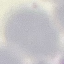
Summary:
  - Malaria status: uninfected
  - Stain: Giemsa
  - Capture: smartphone camera at the microscope eyepiece
  - Preparation: thin blood smear
  - Image type: automatically extracted cell patch, resized to 64 × 64 pixels